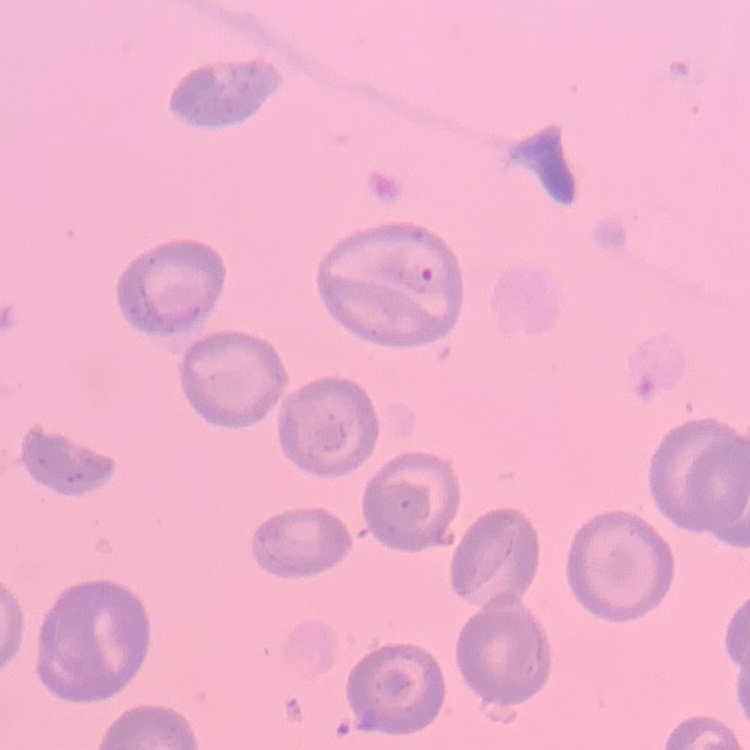
The red blood cells show no rouleaux formation. Thin peripheral smear. Square crop of a larger photomicrograph. Field's or Giemsa stain.